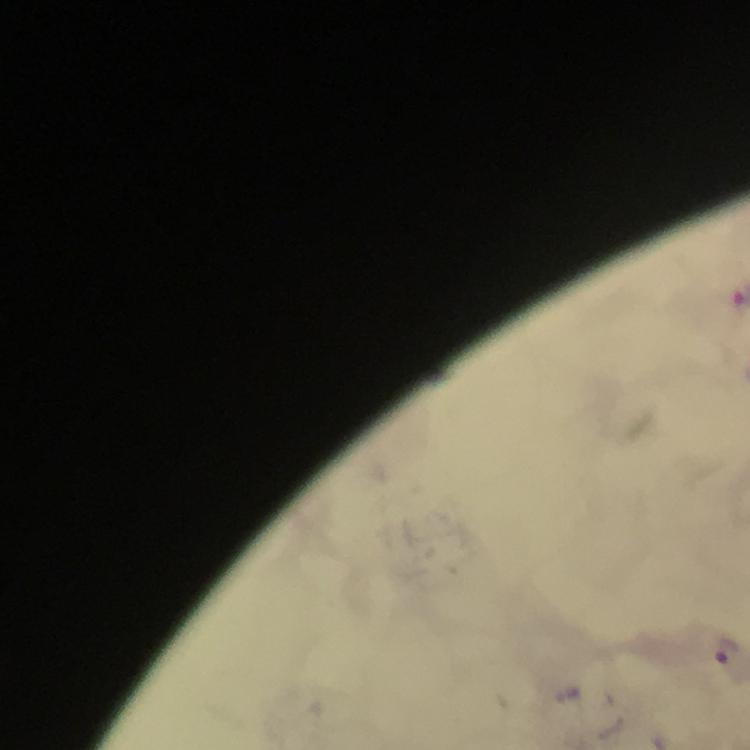 Approximate centers as {x, y} in pixels. Malaria parasite locations: {724, 651}. Photographed through the microscope with a smartphone camera. A crop from one field of view. Giemsa stain. At 100x magnification. Thick blood film. From a diagnostic examination for malaria. Image is 750×750 pixels. Immersion oil was used.